Locate every malaria parasite.
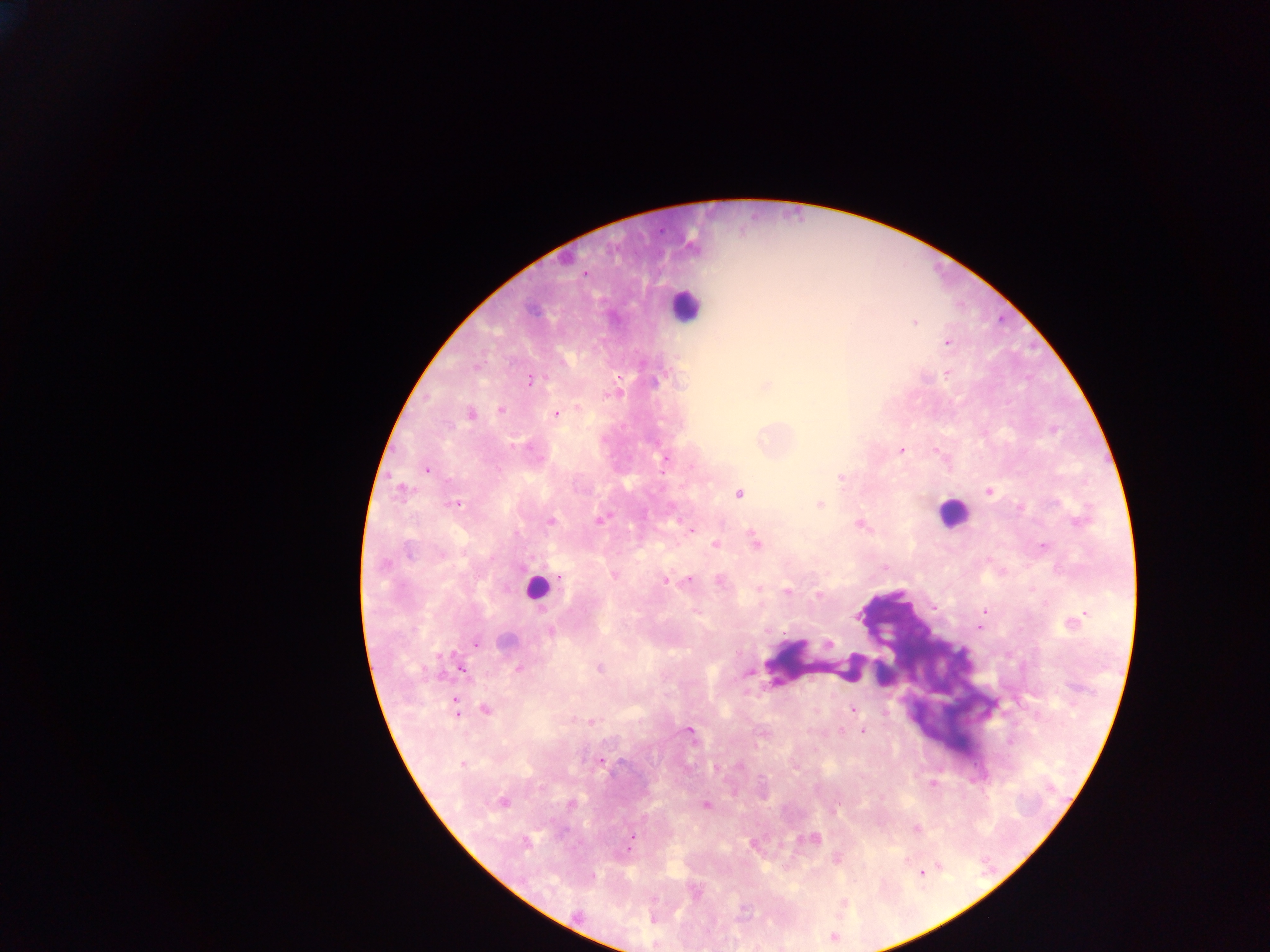

Approximate centers as x y in pixels.
Malaria parasites: 585 273; 914 322; 948 342; 530 380; 655 382; 765 386; 579 407; 500 411; 470 414; 556 414; 901 451; 935 451; 665 459; 427 469; 841 477; 402 490; 989 491; 739 494; 456 504; 820 504; 601 519; 551 522; 859 525; 691 530; 754 539; 715 545; 1043 546; 409 551; 441 555; 614 575; 666 580; 688 580; 719 581; 758 588; 788 591; 818 595; 935 607; 984 611; 979 628; 550 632; 506 642; 829 643; 476 644; 518 668; 600 668; 461 669; 748 672; 454 706; 485 709; 851 709; 592 721; 690 730; 841 731; 863 731; 601 761; 462 764; 933 784; 503 801; 571 804; 706 805; 916 828; 633 836; 809 838; 525 842; 923 874; 592 875; 576 914.

Leukocyte locations: 685 306; 952 513; 535 589; 816 663. Sample from Ghana. Single field of view. Mobile-phone photograph taken through the microscope. Image is 1270×952 pixels. Thick blood film.